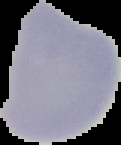
malaria_status: uninfected
image_type: segmented cell region on a black background
preparation: thin blood film
image_size: 121×145 pixels